Name the blood parasite species.
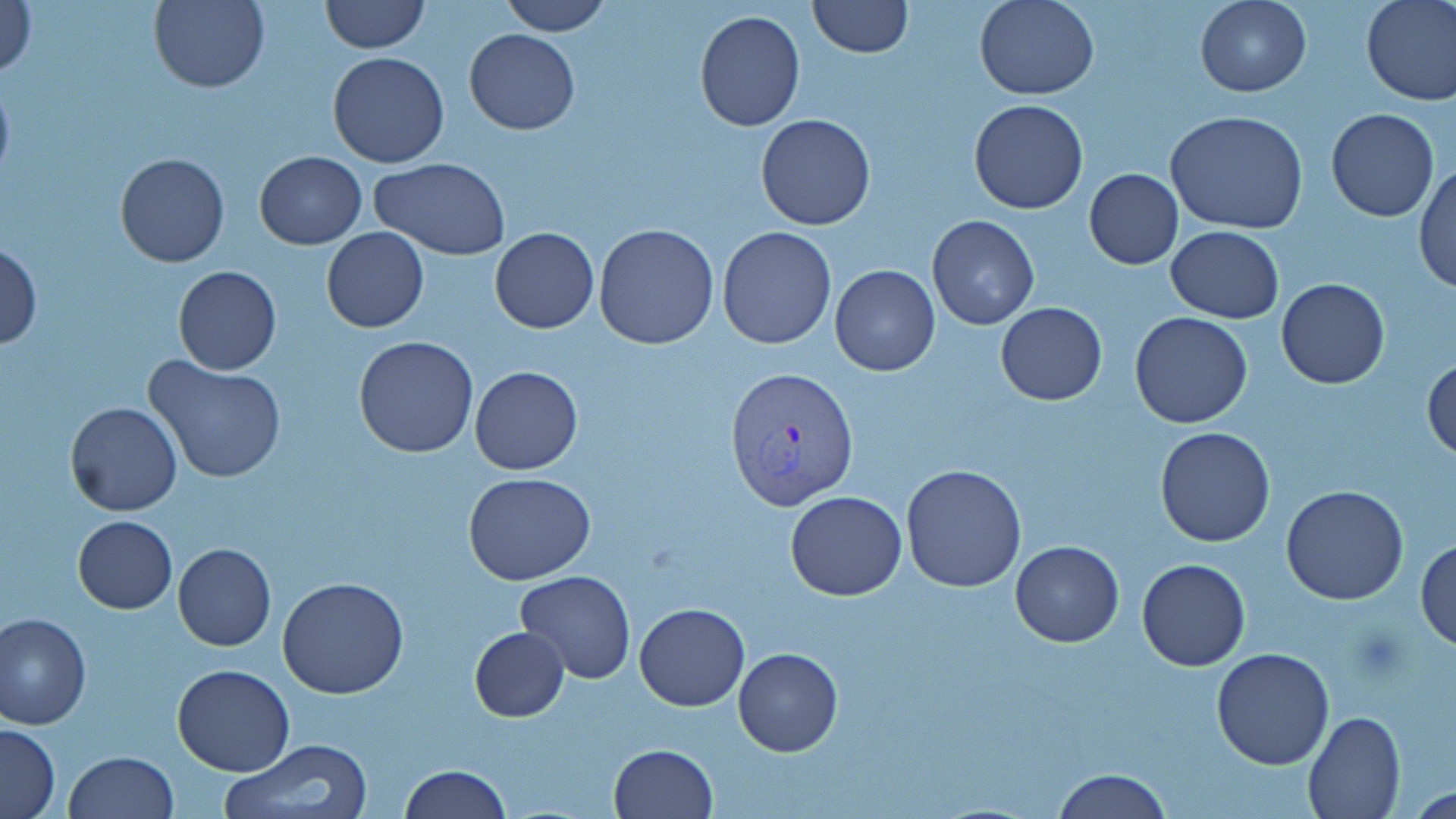
Plasmodium vivax.

Summary:
  - Coordinate format: approximate bounding boxes as named x1/y1/x2/y2 corners in pixels
  - Plasmodium vivax-infected red blood cell locations: (x1=722, y1=364, x2=859, y2=509)
  - Uninfected red blood cell locations: (x1=1, y1=0, x2=37, y2=81), (x1=150, y1=0, x2=270, y2=93), (x1=498, y1=0, x2=612, y2=37), (x1=974, y1=0, x2=1100, y2=100), (x1=1194, y1=0, x2=1312, y2=97), (x1=1361, y1=0, x2=1456, y2=105), (x1=321, y1=1, x2=431, y2=53), (x1=805, y1=1, x2=914, y2=58), (x1=693, y1=9, x2=807, y2=132), (x1=464, y1=29, x2=579, y2=134), (x1=327, y1=51, x2=450, y2=168), (x1=0, y1=75, x2=14, y2=187), (x1=969, y1=100, x2=1089, y2=215), (x1=1164, y1=109, x2=1308, y2=235), (x1=1326, y1=109, x2=1438, y2=222), (x1=756, y1=112, x2=876, y2=231), (x1=114, y1=151, x2=231, y2=268), (x1=254, y1=151, x2=366, y2=249), (x1=367, y1=157, x2=511, y2=259), (x1=1413, y1=160, x2=1456, y2=296), (x1=1084, y1=168, x2=1184, y2=269), (x1=927, y1=214, x2=1038, y2=330), (x1=593, y1=223, x2=720, y2=350), (x1=1165, y1=225, x2=1285, y2=324), (x1=717, y1=226, x2=836, y2=348), (x1=321, y1=227, x2=429, y2=332), (x1=490, y1=227, x2=598, y2=333), (x1=1, y1=241, x2=42, y2=350), (x1=829, y1=265, x2=940, y2=376), (x1=173, y1=266, x2=281, y2=375), (x1=1276, y1=278, x2=1390, y2=389), (x1=995, y1=303, x2=1108, y2=405), (x1=1130, y1=311, x2=1253, y2=429), (x1=353, y1=335, x2=479, y2=459), (x1=144, y1=356, x2=287, y2=484), (x1=1423, y1=356, x2=1456, y2=461), (x1=469, y1=366, x2=584, y2=475), (x1=64, y1=401, x2=182, y2=517), (x1=1154, y1=425, x2=1277, y2=548), (x1=900, y1=463, x2=1028, y2=593), (x1=464, y1=472, x2=596, y2=584), (x1=1280, y1=485, x2=1409, y2=605), (x1=785, y1=489, x2=907, y2=601), (x1=72, y1=514, x2=177, y2=614), (x1=1415, y1=537, x2=1456, y2=654), (x1=1011, y1=541, x2=1124, y2=648), (x1=173, y1=543, x2=275, y2=652), (x1=1137, y1=558, x2=1251, y2=670), (x1=515, y1=571, x2=635, y2=682), (x1=277, y1=576, x2=409, y2=700), (x1=633, y1=604, x2=749, y2=712), (x1=1, y1=612, x2=92, y2=729), (x1=469, y1=625, x2=570, y2=721), (x1=733, y1=647, x2=843, y2=757), (x1=1210, y1=647, x2=1335, y2=770), (x1=171, y1=663, x2=296, y2=776), (x1=1301, y1=709, x2=1406, y2=818), (x1=0, y1=722, x2=61, y2=817), (x1=219, y1=739, x2=373, y2=819), (x1=607, y1=743, x2=718, y2=818), (x1=64, y1=750, x2=178, y2=819), (x1=397, y1=764, x2=510, y2=818), (x1=1051, y1=769, x2=1171, y2=819)
  - Preparation: thin blood smear
  - Image size: 1456×819 pixels
  - Magnification: 1000x
  - Modality: light microscopy
  - Stain: May-Grünwald-Giemsa
  - Field of view: single